Assess this cell for malaria.
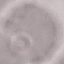
It is uninfected.

Thin blood smear. Photographed with a smartphone camera at the microscope eyepiece. Giemsa-stained preparation. Automatically extracted cell patch, resized to 64 × 64 pixels.